Name the parasite shown.
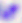
Toxoplasma gondii.

Micrograph. 400x magnification.